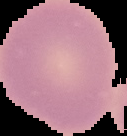

Result: no Plasmodium parasites seen. Segmented cell region on a black background. From a thin blood smear. Image is 127×136 pixels.